Report the malaria status of this cell.
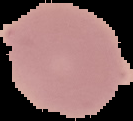
Uninfected.

Image is 133×121 pixels. From a thin blood film. The area outside the segmented cell region is set to black.